Identify the preparation type.
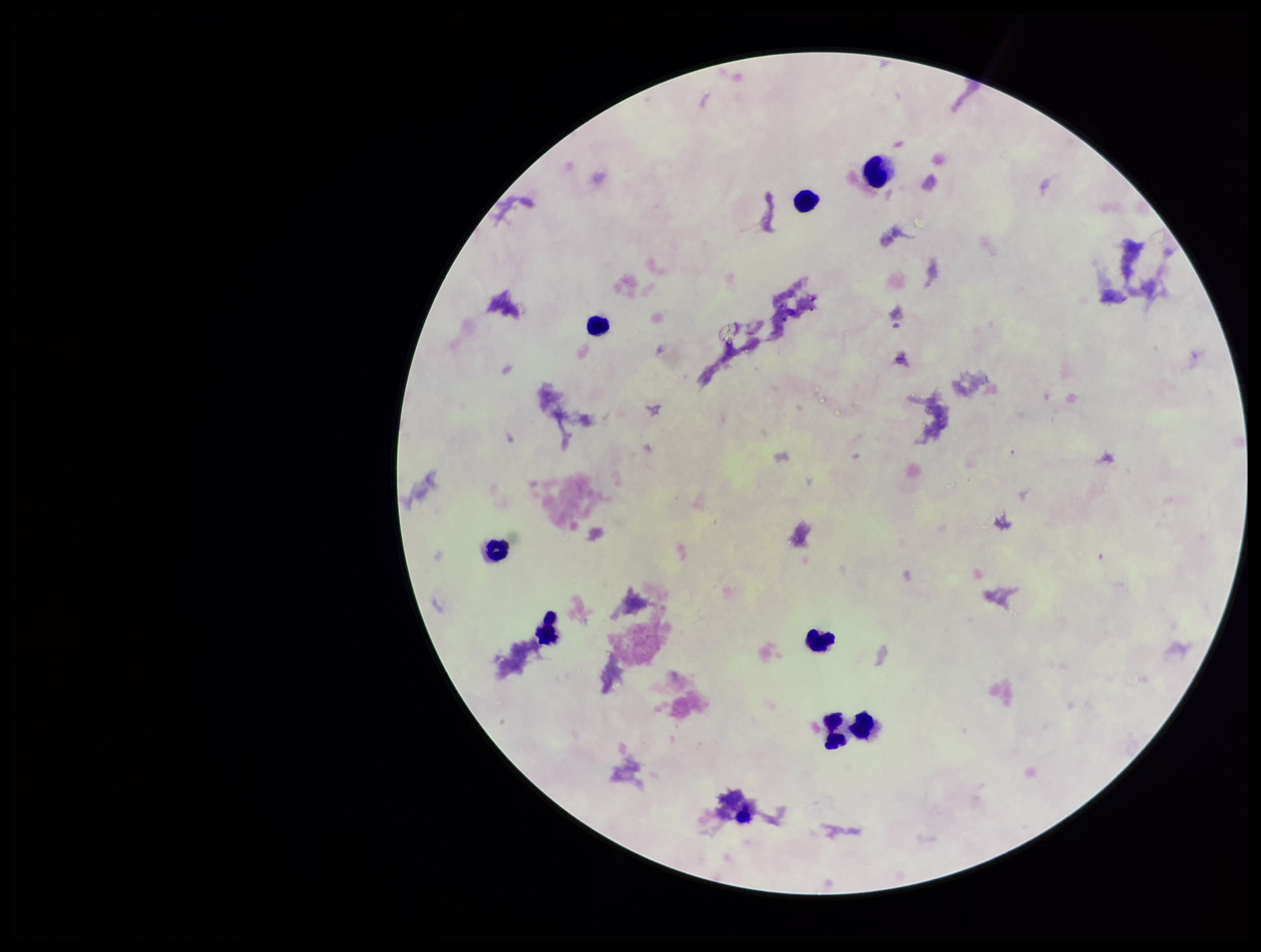

Thick.

Summary:
  - Patient malaria status: negative
  - Capture: smartphone photograph through the microscope eyepiece
  - Plasmodium parasites: none identified
  - Stain: Giemsa
  - Parasite count: 0
  - Leukocyte count: 9
  - Image size: 1261×952 pixels
  - Field of view: single